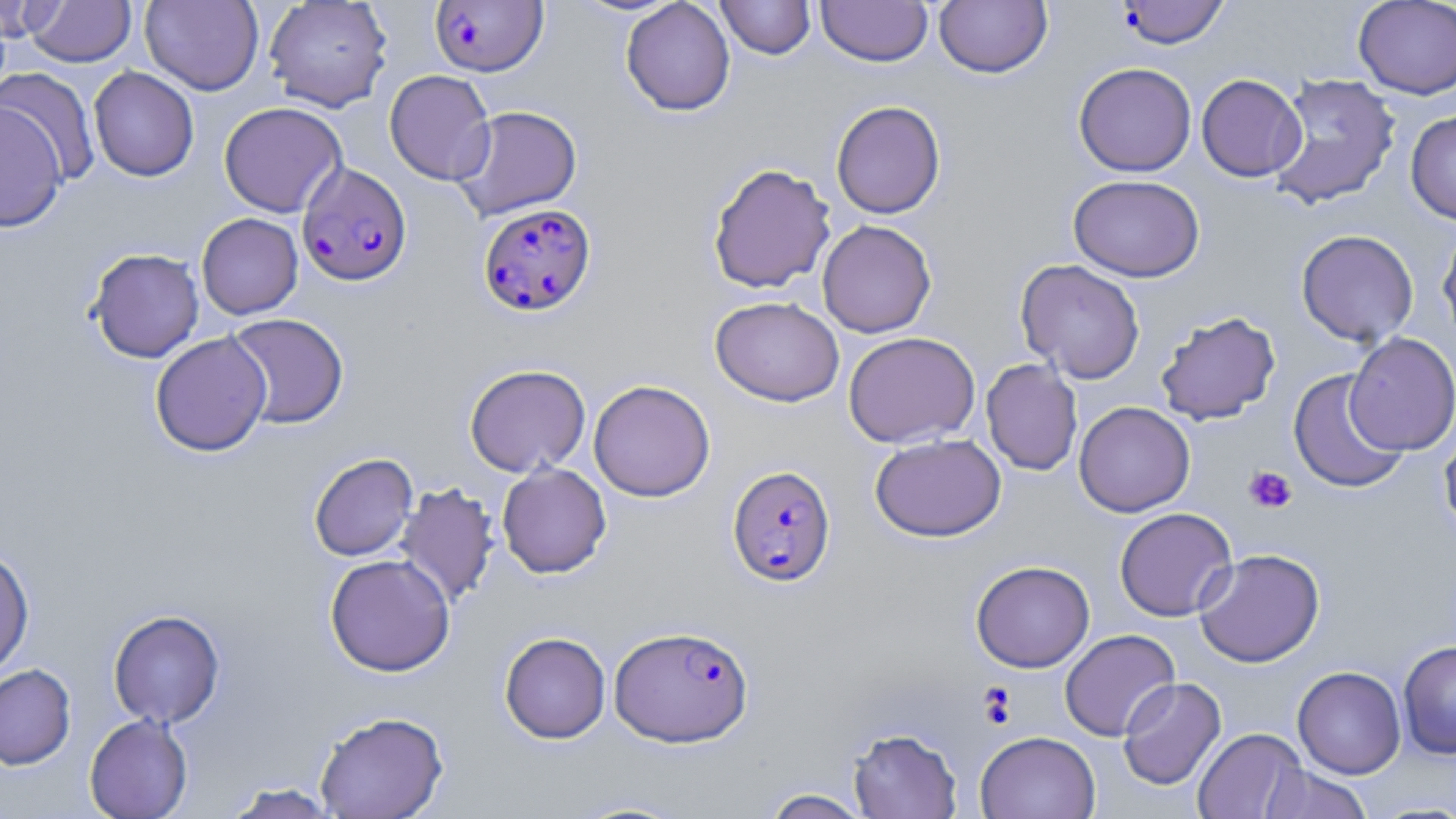
Summary:
  - Coordinate format: approximate bounding boxes as (x1, y1, x2, y2) in pixels
  - Uninfected red blood cell locations: (140, 0, 264, 95), (620, 0, 736, 116), (716, 0, 816, 60), (816, 0, 933, 67), (1353, 0, 1456, 99), (25, 1, 136, 67), (264, 1, 392, 112), (934, 1, 1052, 78), (0, 2, 59, 42), (1073, 62, 1197, 177), (88, 66, 199, 182), (0, 67, 101, 185), (384, 69, 496, 185), (1267, 73, 1402, 210), (1196, 74, 1306, 182), (831, 100, 946, 219), (0, 101, 68, 234), (219, 101, 347, 217), (451, 104, 583, 221), (1405, 109, 1456, 224), (707, 162, 836, 294), (1068, 174, 1205, 282), (196, 213, 303, 319), (816, 219, 937, 338), (1437, 223, 1456, 345), (1296, 229, 1419, 347), (86, 247, 205, 362), (1015, 259, 1146, 384), (710, 296, 845, 406), (1155, 310, 1281, 425), (225, 313, 349, 429), (150, 331, 272, 456), (843, 331, 980, 448), (1344, 332, 1456, 455), (981, 358, 1083, 476), (464, 363, 591, 478), (1287, 369, 1409, 495), (588, 379, 715, 502), (1073, 401, 1195, 517), (1438, 423, 1456, 539), (870, 433, 1006, 542), (308, 453, 418, 561), (496, 462, 612, 578), (394, 482, 500, 608), (1114, 507, 1238, 622), (0, 547, 35, 678), (1194, 548, 1325, 667), (324, 553, 455, 677), (970, 560, 1095, 672), (108, 609, 225, 728), (1059, 629, 1179, 742), (499, 632, 611, 743), (1398, 639, 1456, 759), (0, 664, 76, 769), (1292, 665, 1406, 779), (1117, 676, 1226, 791), (314, 711, 449, 818), (84, 713, 194, 819), (848, 727, 963, 818), (1192, 728, 1306, 819), (975, 730, 1100, 819), (1259, 764, 1374, 819), (221, 782, 344, 818), (760, 788, 874, 818), (566, 797, 695, 817)
  - Plasmodium falciparum-infected red blood cell locations: (1115, 1, 1230, 48), (430, 2, 551, 80), (297, 161, 411, 286), (478, 203, 597, 317), (726, 464, 836, 586), (610, 624, 754, 747)
  - Platelet locations: (1243, 465, 1297, 514), (978, 684, 1017, 727)
  - Slide-level diagnosis: Plasmodium falciparum
  - Magnification: 1000x
  - Preparation: thin blood film
  - Image size: 1456×819 pixels
  - Field of view: one of a larger specimen
  - Modality: light microscopy
  - Stain: May-Grünwald-Giemsa